Name the parasite shown.
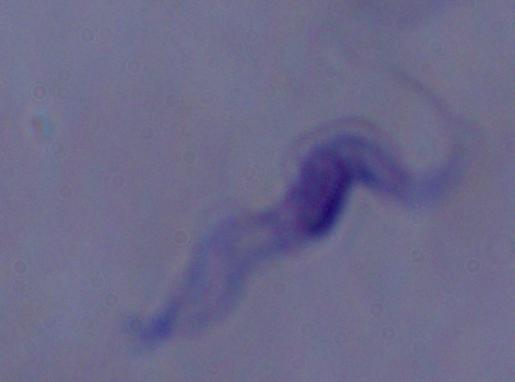
This is a trypanosome.

Micrograph. Captured at 1000x magnification.